Assess the morphology of the erythrocytes.
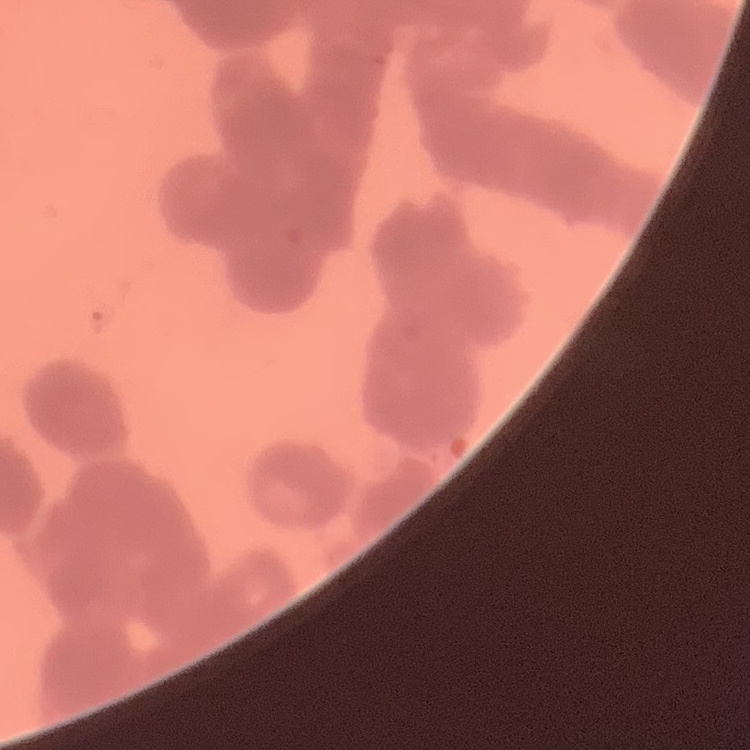
They show rouleaux formation.

Summary:
  - Stain: Field's or Giemsa
  - Preparation: thin blood smear
  - Image type: square crop of a larger photomicrograph